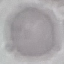

Malaria status: uninfected. Giemsa stain. Automatically extracted cell patch, resized to 64 × 64 pixels. Thin blood smear. Acquired by smartphone through the microscope eyepiece.